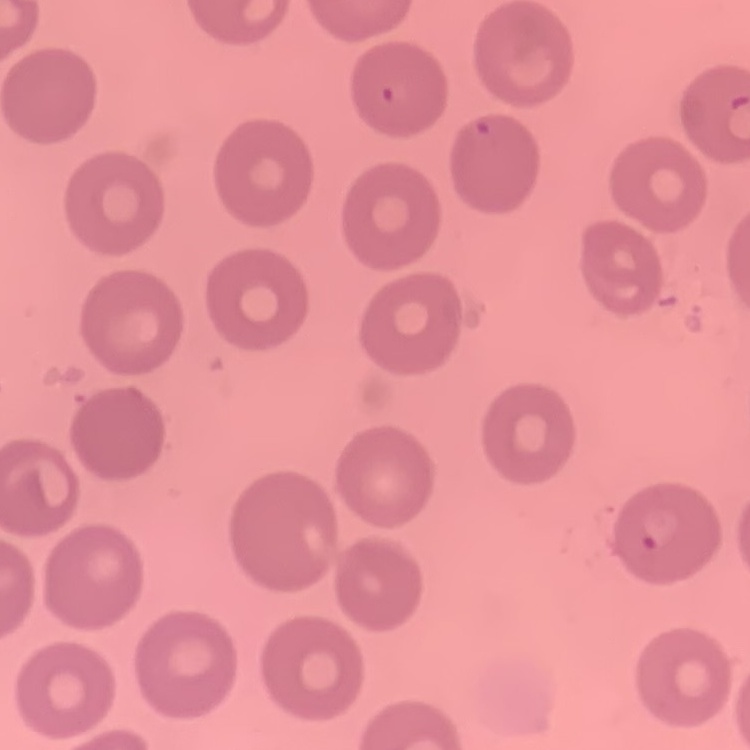
Summary:
  - Red blood cell morphology: no rouleaux formation
  - Preparation: thin blood smear
  - Image type: square crop of a larger photomicrograph
  - Stain: Field's or Giemsa